State which parasite is depicted.
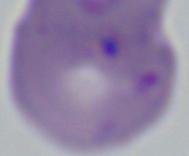

This is Babesia.

Photomicrograph. Captured at 1000x magnification.